Classify this cell by malaria status.
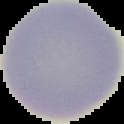

Uninfected.

Summary:
  - Image size: 124×124 pixels
  - Preparation: thin blood smear
  - Image type: cell region segmented out of the field of view; surrounding area masked to black